Point out each Plasmodium parasite.
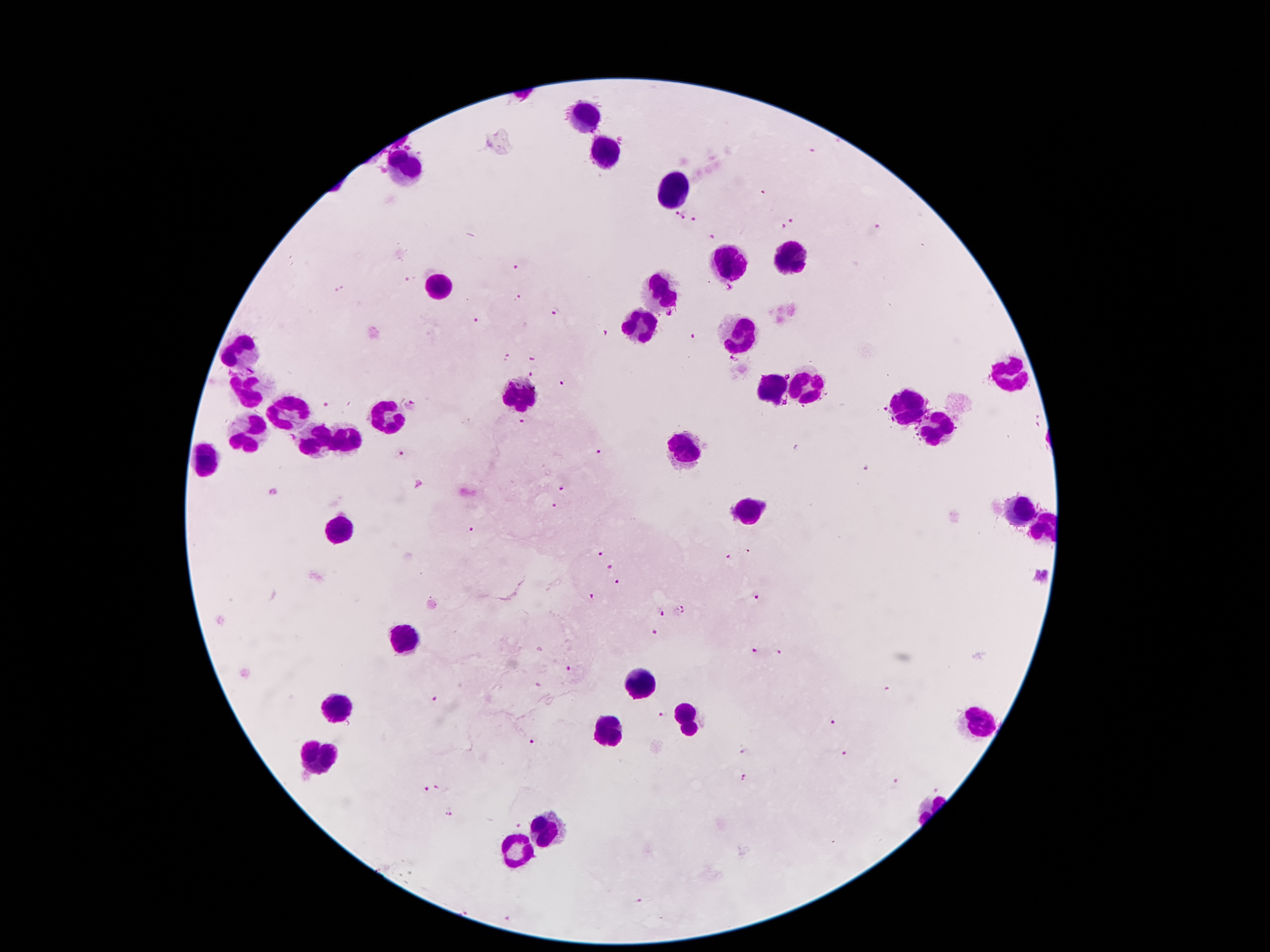

Approximate object centers, in pixels from the top-left corner.
Plasmodium parasites: (x=837, y=142), (x=810, y=153), (x=764, y=193), (x=676, y=212), (x=684, y=215), (x=695, y=220), (x=793, y=221), (x=782, y=229), (x=876, y=229), (x=713, y=237), (x=515, y=270), (x=408, y=280), (x=339, y=290), (x=517, y=296), (x=556, y=311), (x=476, y=320), (x=607, y=332), (x=694, y=336), (x=505, y=359), (x=532, y=359), (x=531, y=374), (x=561, y=384), (x=325, y=404), (x=410, y=405), (x=523, y=422), (x=401, y=452), (x=597, y=453), (x=869, y=468), (x=564, y=488), (x=273, y=491), (x=554, y=506), (x=473, y=529), (x=598, y=553), (x=727, y=558), (x=610, y=569), (x=616, y=581), (x=592, y=595), (x=756, y=595), (x=680, y=610), (x=659, y=612), (x=655, y=633), (x=755, y=650), (x=779, y=653), (x=572, y=671), (x=885, y=687), (x=435, y=699), (x=664, y=714), (x=833, y=722), (x=532, y=742), (x=745, y=750), (x=844, y=752), (x=742, y=781), (x=896, y=782), (x=443, y=787), (x=936, y=788), (x=426, y=790), (x=448, y=814), (x=516, y=825), (x=640, y=902), (x=469, y=910), (x=507, y=917).

Leukocyte locations: (x=586, y=113), (x=604, y=151), (x=402, y=167), (x=672, y=193), (x=790, y=255), (x=726, y=265), (x=440, y=285), (x=662, y=290), (x=638, y=323), (x=738, y=340), (x=240, y=352), (x=1010, y=375), (x=804, y=382), (x=772, y=388), (x=250, y=392), (x=522, y=398), (x=906, y=404), (x=388, y=412), (x=288, y=416), (x=932, y=428), (x=348, y=436), (x=250, y=440), (x=322, y=442), (x=678, y=452), (x=1022, y=512), (x=744, y=514), (x=342, y=526), (x=406, y=640), (x=638, y=684), (x=338, y=710), (x=684, y=722), (x=976, y=722), (x=606, y=736), (x=316, y=758), (x=546, y=828), (x=516, y=852). Image is 1270×952 pixels. Single field of view. Photographed through the microscope eyepiece with a smartphone camera. Giemsa-stained preparation. Patient malaria status: infected with Plasmodium falciparum. 100x magnification. Thick blood film.